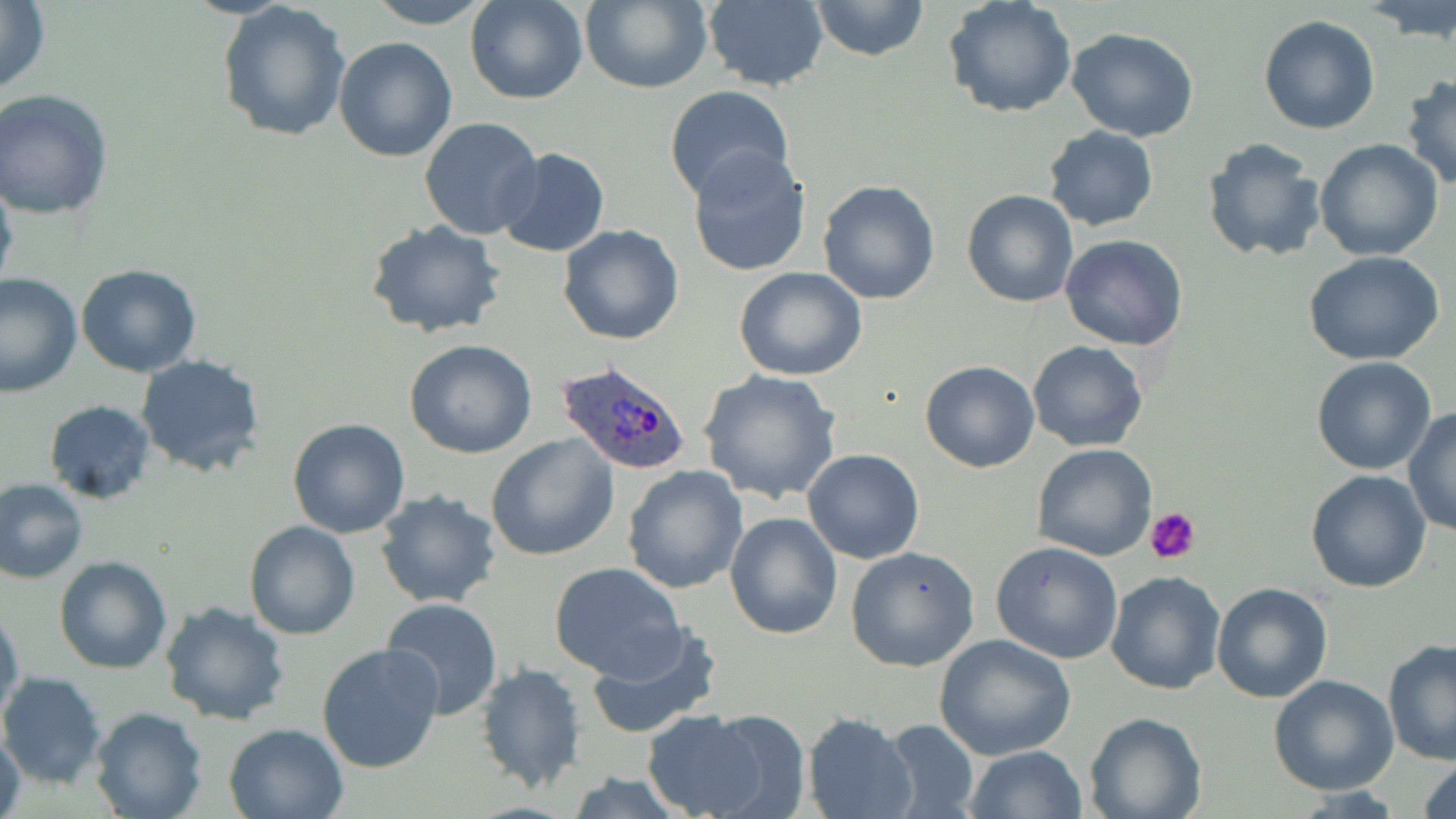

{
  "slide_level_diagnosis": "Plasmodium ovale",
  "platelet_locations": "approximate bounding boxes as (x1,y1)-(x2,y2) corner pairs in pixels: (1146,505)-(1203,564)",
  "magnification": "1000x",
  "stain": "May-Grünwald-Giemsa",
  "field_of_view": "single",
  "preparation": "thin blood smear",
  "uninfected_red_blood_cell_locations": "approximate bounding boxes as (x1,y1)-(x2,y2) corner pairs in pixels: (0,0)-(51,96), (367,0)-(492,27), (466,0)-(589,104), (580,0)-(713,95), (808,0)-(929,60), (943,0)-(1078,119), (1364,0)-(1456,43), (216,1)-(352,143), (700,1)-(828,90), (1259,14)-(1380,134), (1066,27)-(1201,143), (334,35)-(457,161), (1403,73)-(1456,191), (663,85)-(797,207), (0,90)-(115,218), (419,118)-(543,239), (1044,127)-(1159,230), (1200,138)-(1326,263), (1313,139)-(1443,261), (495,147)-(610,259), (687,148)-(813,276), (0,171)-(19,303), (818,180)-(940,303), (961,189)-(1079,308), (366,219)-(506,339), (557,225)-(686,346), (1059,235)-(1188,353), (1303,250)-(1446,365), (76,264)-(203,377), (734,267)-(869,381), (0,271)-(82,396), (404,340)-(537,459), (1027,340)-(1148,452), (137,355)-(266,477), (1312,357)-(1438,475), (919,360)-(1040,472), (698,368)-(844,505), (42,399)-(158,505), (1404,408)-(1456,536), (287,418)-(413,538), (486,435)-(619,559), (1030,443)-(1158,561), (804,448)-(926,564), (621,465)-(749,594), (1305,468)-(1433,593), (1,477)-(88,584), (375,490)-(503,609), (724,511)-(844,640), (245,520)-(359,640), (991,540)-(1125,664), (845,545)-(981,671), (55,556)-(171,673), (548,560)-(687,681), (1104,569)-(1228,695), (1210,581)-(1332,703), (381,598)-(503,719), (160,600)-(293,726), (0,605)-(22,724), (584,623)-(722,741), (933,633)-(1076,760), (1382,641)-(1456,767), (317,642)-(446,775), (476,663)-(588,795), (0,672)-(107,789), (1268,674)-(1399,795), (90,707)-(208,819), (694,707)-(812,816), (643,710)-(772,818), (1084,712)-(1205,819), (803,714)-(917,819), (882,719)-(979,819), (223,721)-(349,818), (1,730)-(25,819), (964,745)-(1088,819), (1418,756)-(1456,819), (564,773)-(690,818)",
  "image_size": "1456×819 pixels",
  "plasmodium_ovale_infected_red_blood_cell_locations": "approximate bounding boxes as (x1,y1)-(x2,y2) corner pairs in pixels: (555,358)-(694,476)",
  "modality": "light microscopy"
}